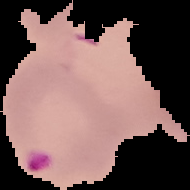
Summary:
  - Image type: cell region segmented out of the field of view; surrounding area masked to black
  - Preparation: thin blood smear
  - Malaria status: parasitized
  - Image size: 190×190 pixels